Assess this cell for malaria.
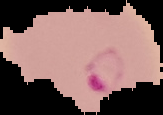

Parasitized.

image size = 163×115 pixels
image type = segmented cell region with the area outside set to black
preparation = thin blood film